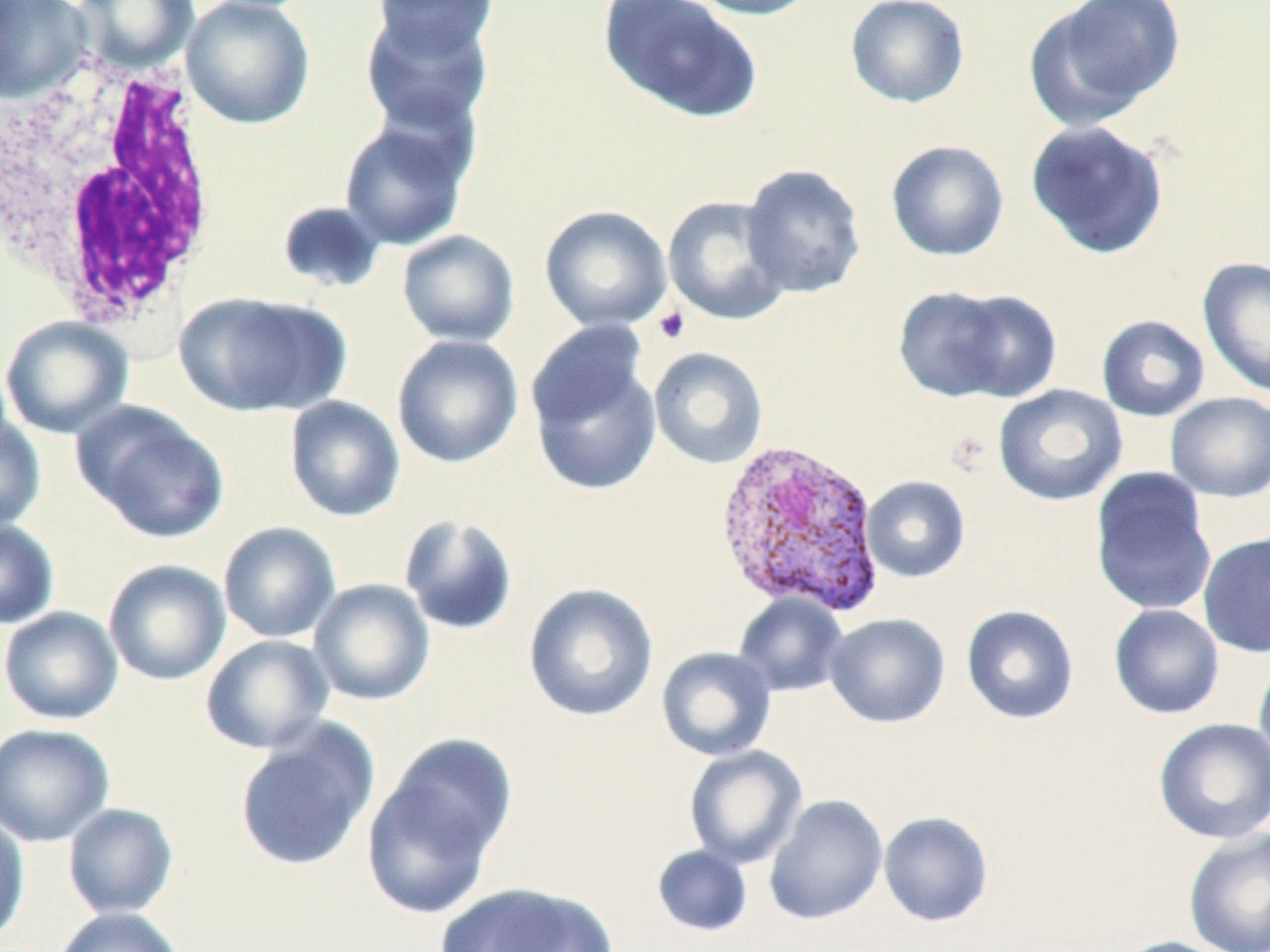

{
  "slide_level_diagnosis": "Plasmodium vivax",
  "modality": "light microscopy",
  "uninfected_red_blood_cell_locations": "approximate bounding boxes as [x1, y1, x2, y2] in pixels: [0, 0, 92, 105], [72, 0, 199, 72], [181, 0, 317, 130], [371, 0, 498, 59], [596, 0, 763, 124], [684, 0, 822, 20], [846, 0, 970, 109], [1025, 0, 1185, 129], [360, 7, 497, 136], [338, 116, 474, 251], [1025, 120, 1170, 260], [885, 139, 1010, 262], [740, 163, 868, 299], [662, 195, 793, 326], [275, 200, 386, 295], [539, 204, 673, 332], [396, 229, 520, 347], [1197, 256, 1270, 398], [893, 285, 1022, 402], [943, 289, 1063, 402], [173, 290, 345, 418], [1096, 314, 1210, 422], [0, 316, 134, 439], [391, 334, 524, 469], [527, 344, 663, 496], [649, 346, 769, 469], [993, 384, 1128, 507], [1165, 392, 1270, 502], [284, 396, 405, 522], [71, 400, 231, 544], [0, 413, 46, 533], [1089, 469, 1217, 616], [861, 475, 971, 583], [398, 513, 520, 637], [0, 521, 59, 629], [218, 521, 340, 643], [1198, 531, 1270, 658], [103, 559, 231, 686], [308, 579, 435, 707], [523, 583, 659, 723], [732, 593, 849, 698], [961, 604, 1080, 725], [1108, 604, 1225, 720], [0, 606, 124, 725], [825, 613, 951, 728], [200, 635, 334, 755], [656, 646, 777, 761], [1253, 652, 1270, 777], [1152, 717, 1270, 844], [233, 720, 379, 873], [0, 722, 115, 848], [361, 738, 515, 919], [684, 745, 808, 869], [764, 795, 889, 925], [62, 802, 179, 919], [0, 811, 30, 947], [878, 811, 994, 927], [1183, 828, 1270, 952], [651, 844, 753, 937], [434, 882, 618, 951], [52, 907, 185, 952], [1109, 936, 1237, 952]",
  "platelet_locations": "approximate bounding boxes as [x1, y1, x2, y2] in pixels: [652, 304, 690, 344]",
  "image_size": "1270×952 pixels",
  "field_of_view": "single",
  "magnification": "1000x",
  "stain": "May-Grünwald-Giemsa",
  "plasmodium_vivax_infected_red_blood_cell_locations": "approximate bounding boxes as [x1, y1, x2, y2] in pixels: [713, 438, 886, 619]",
  "white_blood_cell_locations": "approximate bounding boxes as [x1, y1, x2, y2] in pixels: [2, 41, 223, 332]",
  "preparation": "thin blood smear"
}